Assess this cell for malaria.
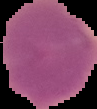

Uninfected.

Image is 97×109 pixels. From a thin blood film. The area outside the segmented cell region is set to black.